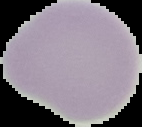

Segmented cell region on a black background. Malaria status: uninfected. From a thin blood film. Image is 142×127 pixels.